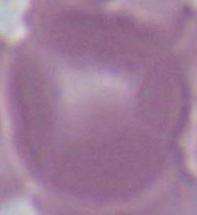
identification = red blood cell
modality = micrograph
magnification = 1000x